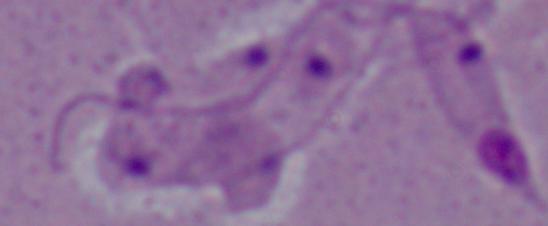
Summary:
  - Identification: Leishmania
  - Magnification: 1000x
  - Modality: micrograph